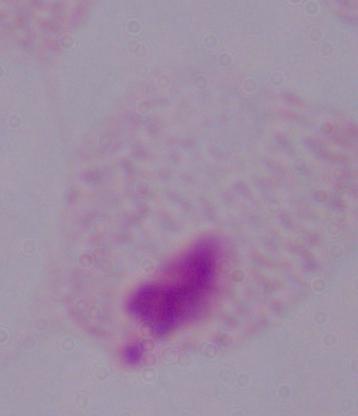
Captured at 1000x magnification. A trichomonad is seen. Micrograph.